Assess for parasitized red blood cells.
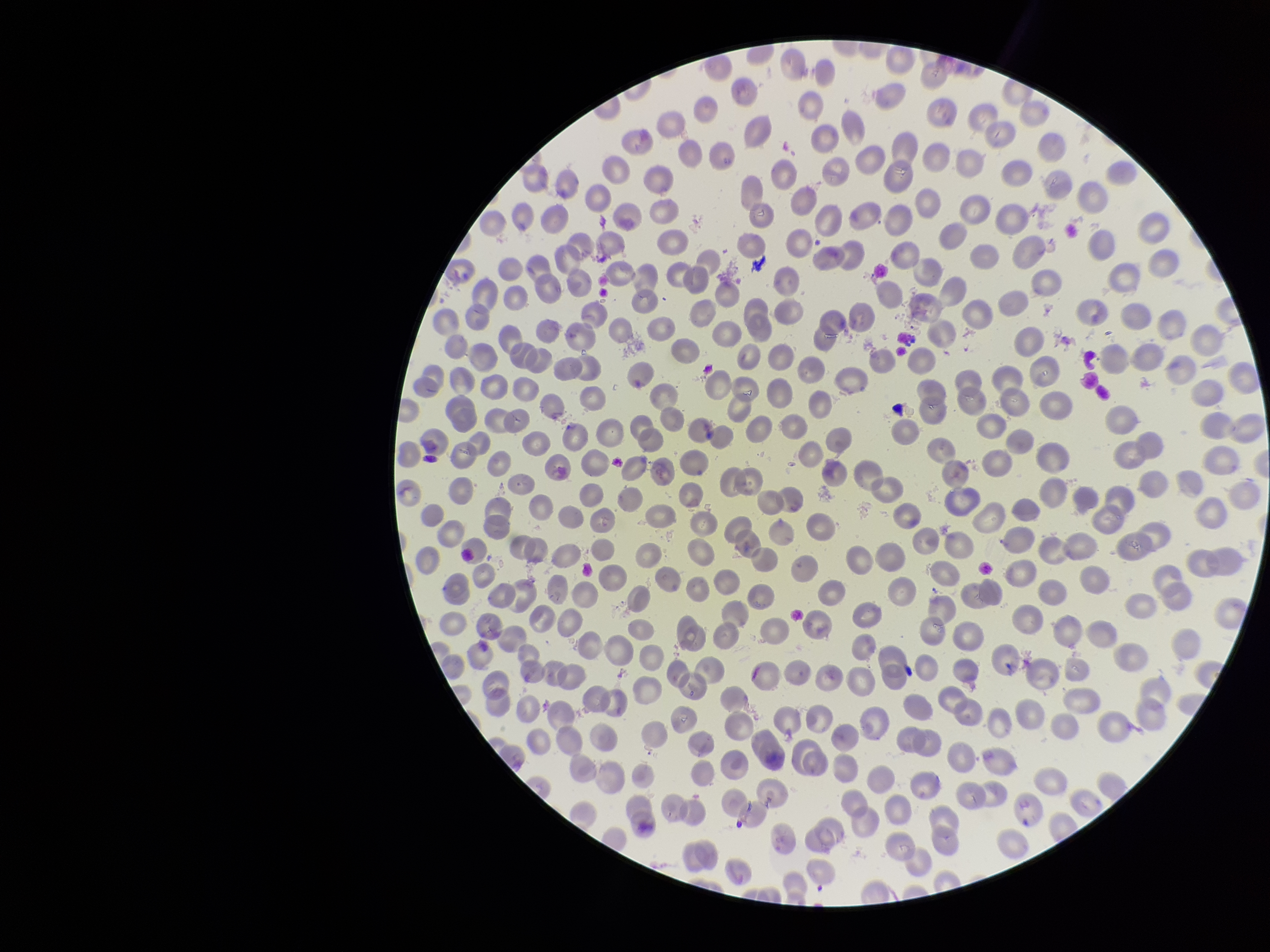
None seen.

Summary:
  - Image size: 1270×952 pixels
  - Red blood cell count: 344
  - Patient malaria status: negative
  - Parasitized red blood cell count: 0
  - Stain: Giemsa
  - Capture: smartphone photograph through the microscope eyepiece
  - Field of view: one from this slide
  - Preparation: thin smear